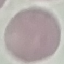

Summary:
  - Result: no malaria parasites seen
  - Capture: smartphone camera at the microscope eyepiece
  - Image type: automatically extracted cell patch, resized to 64 × 64 pixels
  - Preparation: thin blood film
  - Stain: Giemsa